Classify this cell by malaria status.
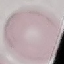

It is uninfected.

Giemsa stain. Photographed with a smartphone camera at the microscope eyepiece. Cell patch, automatically extracted from a larger field of view and resized to 64 × 64 pixels. Thin smear of blood.